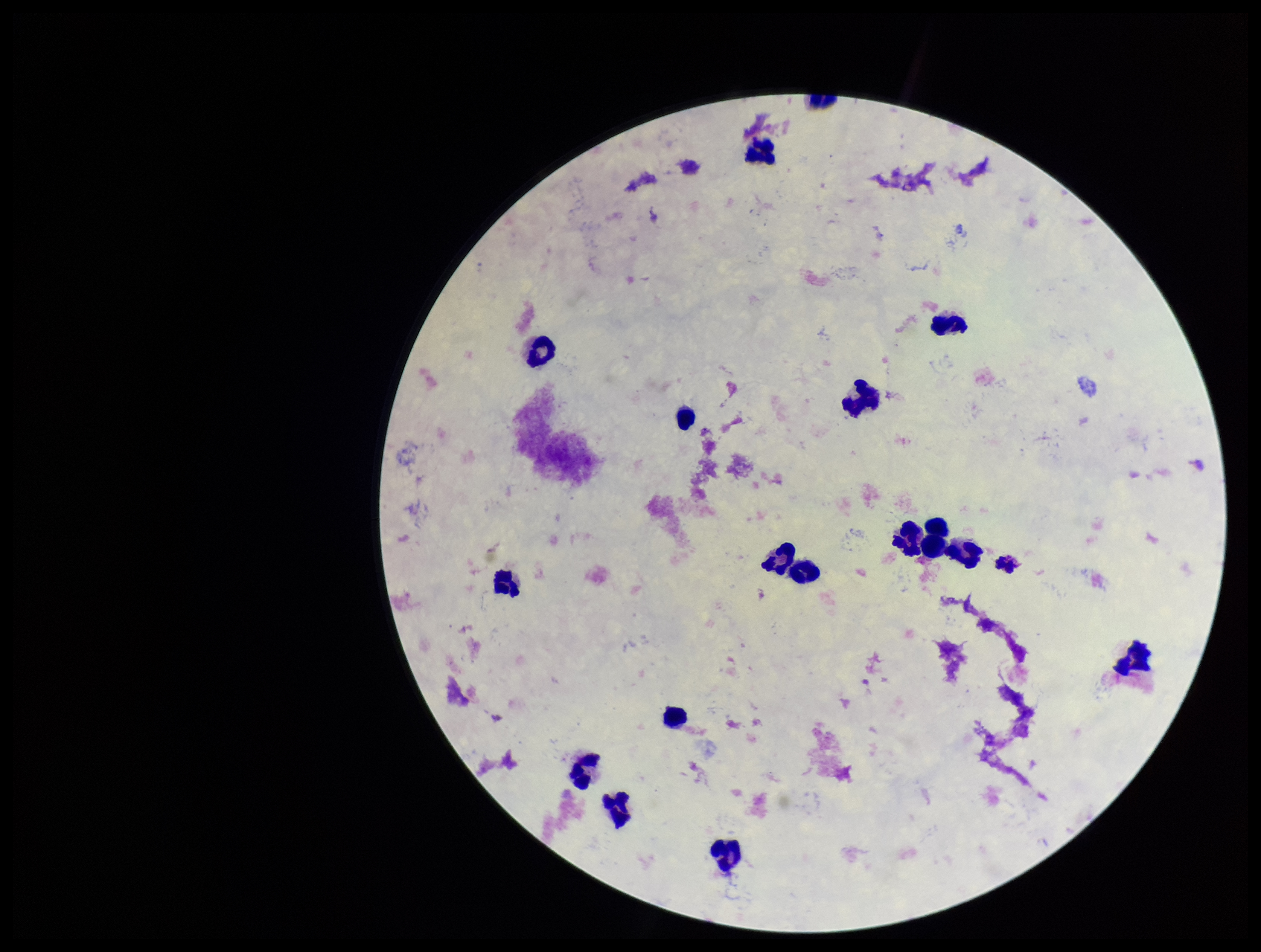

{
  "stain": "Giemsa",
  "plasmodium_parasites": "none detected",
  "parasite_count": 0,
  "image_size": "1261×952 pixels",
  "patient_malaria_status": "negative",
  "leukocyte_count": 17,
  "preparation": "thick",
  "field_of_view": "one from this slide",
  "capture": "smartphone photograph through the microscope eyepiece"
}